Locate and identify every blood parasite.
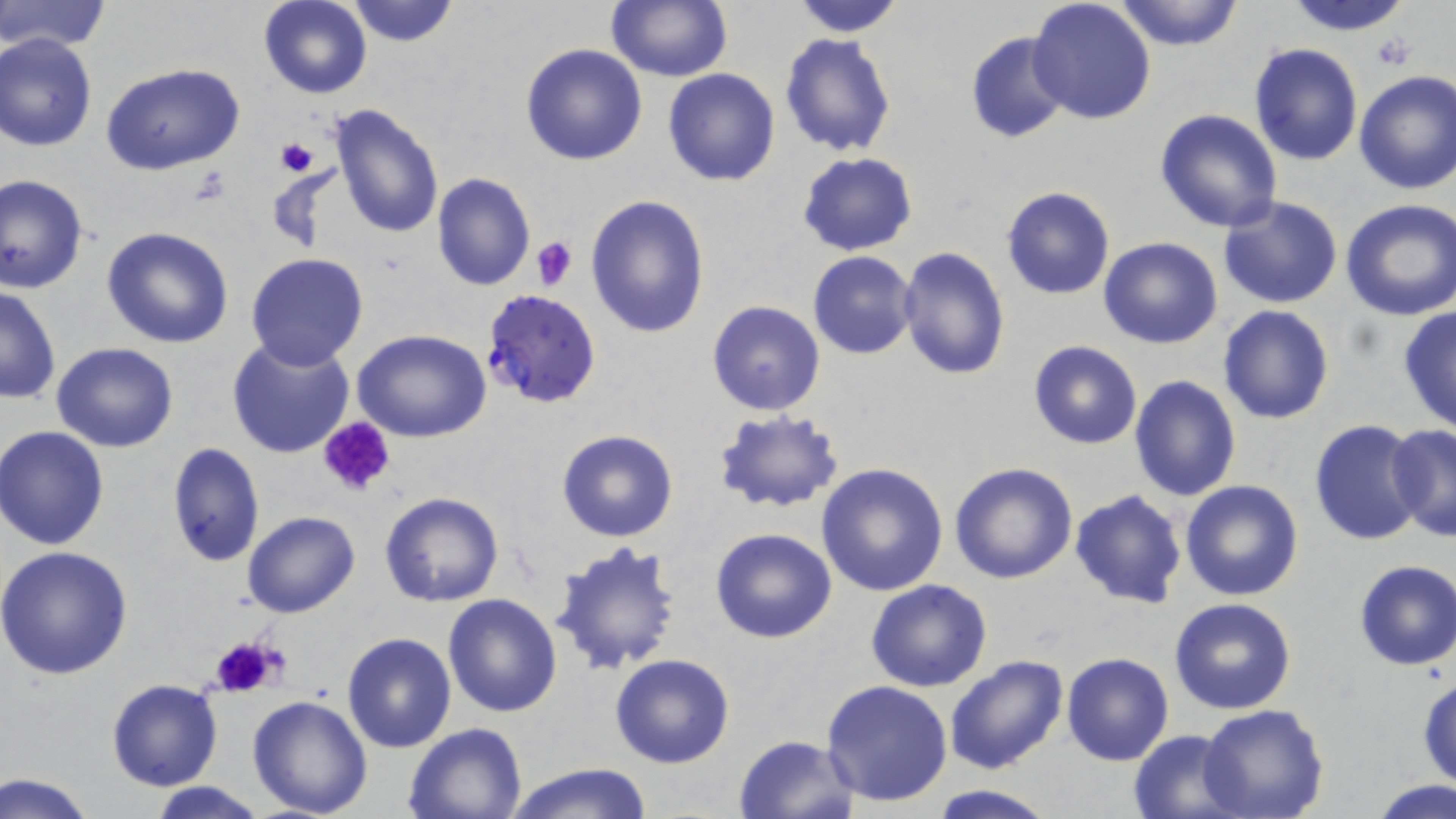

Approximate bounding boxes as named x1/y1/x2/y2 corners in pixels.
Plasmodium falciparum-infected red blood cells: (x1=480, y1=288, x2=602, y2=408).
No Plasmodium ovale, Plasmodium malariae, Plasmodium vivax, Babesia divergens, or Trypanosoma brucei observed.

Platelet locations: (x1=1371, y1=33, x2=1418, y2=70), (x1=274, y1=137, x2=316, y2=177), (x1=184, y1=167, x2=234, y2=206), (x1=531, y1=235, x2=577, y2=291), (x1=318, y1=416, x2=398, y2=499), (x1=209, y1=634, x2=281, y2=695). Uninfected red blood cell locations: (x1=1, y1=0, x2=111, y2=52), (x1=346, y1=0, x2=460, y2=47), (x1=606, y1=0, x2=731, y2=83), (x1=786, y1=0, x2=908, y2=37), (x1=1112, y1=0, x2=1245, y2=52), (x1=1281, y1=0, x2=1421, y2=35), (x1=258, y1=1, x2=372, y2=99), (x1=1027, y1=1, x2=1157, y2=126), (x1=964, y1=31, x2=1072, y2=144), (x1=0, y1=32, x2=97, y2=152), (x1=779, y1=32, x2=896, y2=158), (x1=521, y1=43, x2=648, y2=166), (x1=1248, y1=43, x2=1365, y2=166), (x1=101, y1=63, x2=246, y2=175), (x1=663, y1=68, x2=781, y2=186), (x1=1354, y1=69, x2=1456, y2=195), (x1=329, y1=105, x2=444, y2=242), (x1=1154, y1=107, x2=1283, y2=234), (x1=796, y1=153, x2=917, y2=255), (x1=431, y1=173, x2=537, y2=292), (x1=1, y1=174, x2=89, y2=292), (x1=1000, y1=186, x2=1115, y2=299), (x1=586, y1=195, x2=711, y2=340), (x1=1219, y1=197, x2=1343, y2=309), (x1=1339, y1=198, x2=1456, y2=321), (x1=101, y1=227, x2=234, y2=350), (x1=1097, y1=238, x2=1222, y2=350), (x1=897, y1=247, x2=1010, y2=379), (x1=807, y1=251, x2=917, y2=359), (x1=245, y1=253, x2=368, y2=371), (x1=0, y1=286, x2=61, y2=403), (x1=708, y1=300, x2=825, y2=416), (x1=1397, y1=304, x2=1456, y2=434), (x1=1219, y1=305, x2=1335, y2=425), (x1=354, y1=330, x2=492, y2=442), (x1=225, y1=336, x2=355, y2=460), (x1=1028, y1=341, x2=1143, y2=449), (x1=52, y1=343, x2=179, y2=451), (x1=1129, y1=373, x2=1242, y2=501), (x1=711, y1=409, x2=845, y2=513), (x1=1309, y1=419, x2=1426, y2=545), (x1=1387, y1=422, x2=1456, y2=542), (x1=1, y1=425, x2=113, y2=548), (x1=556, y1=429, x2=680, y2=543), (x1=164, y1=441, x2=264, y2=568), (x1=816, y1=462, x2=949, y2=596), (x1=949, y1=462, x2=1079, y2=585), (x1=1180, y1=480, x2=1303, y2=602), (x1=1068, y1=488, x2=1188, y2=609), (x1=380, y1=491, x2=504, y2=607), (x1=242, y1=510, x2=360, y2=618), (x1=710, y1=527, x2=837, y2=642), (x1=550, y1=538, x2=684, y2=676), (x1=0, y1=546, x2=133, y2=681), (x1=1352, y1=559, x2=1456, y2=670), (x1=867, y1=579, x2=994, y2=692), (x1=443, y1=594, x2=561, y2=717), (x1=1168, y1=599, x2=1296, y2=715), (x1=341, y1=632, x2=456, y2=754), (x1=1061, y1=652, x2=1174, y2=766), (x1=610, y1=654, x2=736, y2=769), (x1=944, y1=654, x2=1067, y2=775), (x1=1418, y1=675, x2=1456, y2=790), (x1=106, y1=679, x2=223, y2=791), (x1=821, y1=679, x2=953, y2=807), (x1=247, y1=694, x2=374, y2=819), (x1=1198, y1=702, x2=1329, y2=819), (x1=403, y1=721, x2=528, y2=818), (x1=1128, y1=729, x2=1242, y2=817), (x1=733, y1=733, x2=859, y2=819), (x1=501, y1=764, x2=654, y2=819), (x1=3, y1=772, x2=95, y2=818), (x1=1370, y1=779, x2=1455, y2=819), (x1=148, y1=782, x2=268, y2=819), (x1=930, y1=785, x2=1053, y2=817). Slide-level diagnosis: Plasmodium falciparum. Optical microscopy. Captured at 1000x magnification. One field of a larger specimen. Image is 1456×819 pixels. Thin blood smear. May-Grünwald-Giemsa-stained preparation.